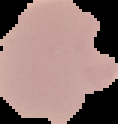 From a thin blood smear. Image is 118×124 pixels. Result: malaria parasites identified. Segmented cell region on a black background.